Give the position of every malaria parasite and every leukocyte.
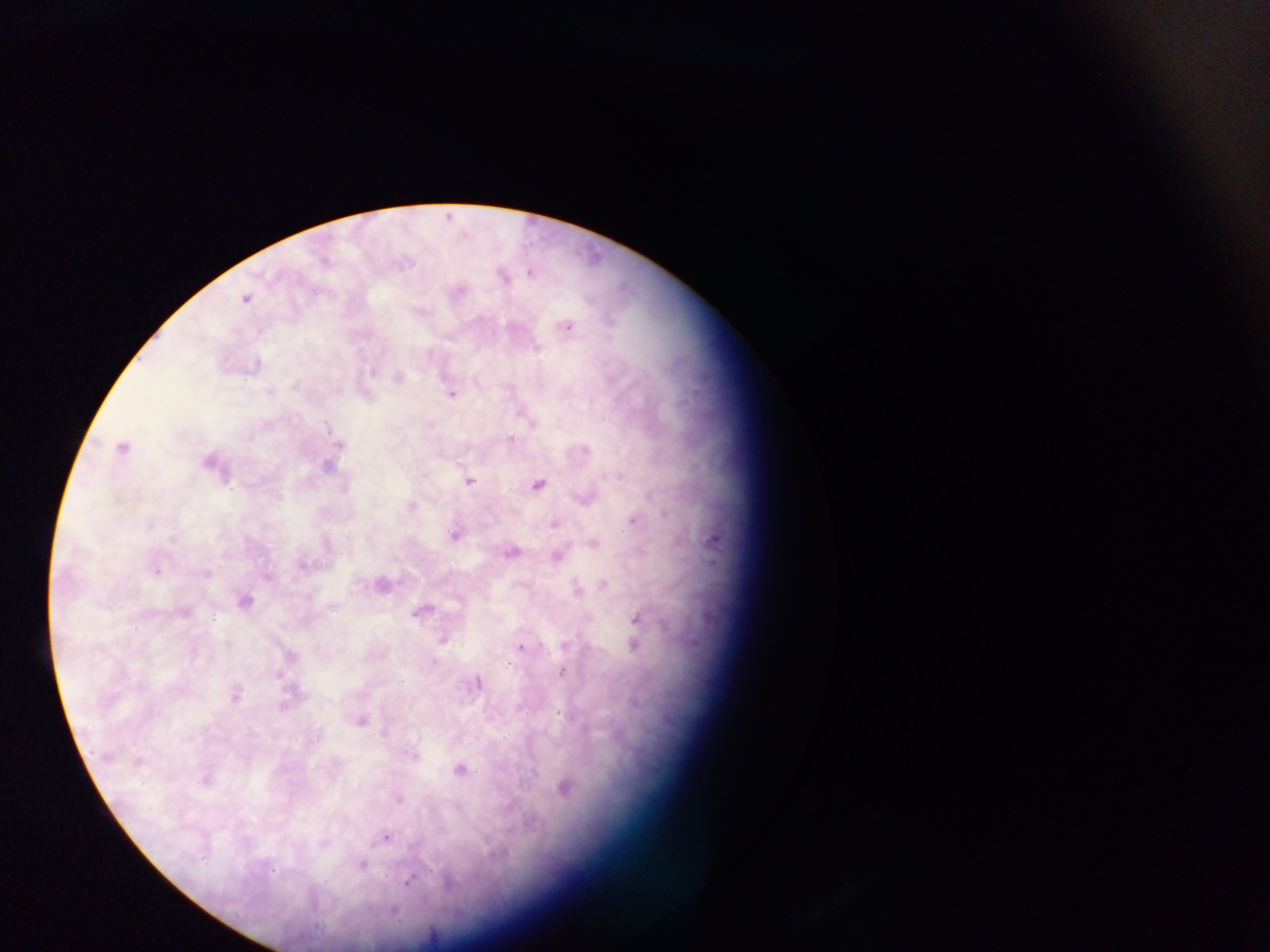
Approximate centers as (x, y) in pixels.
Malaria parasites: (530, 272), (504, 278), (244, 300), (567, 327), (537, 348), (373, 373), (399, 378), (294, 387), (269, 391), (451, 394), (328, 429), (510, 438), (339, 445), (123, 449), (585, 450), (208, 462), (326, 466), (620, 476), (470, 481), (539, 485), (410, 507), (633, 521), (150, 524), (554, 524), (454, 535), (348, 537), (173, 539), (593, 543), (512, 553), (557, 556), (302, 565), (156, 571), (206, 573), (267, 577), (603, 585), (577, 592), (244, 601), (332, 607), (184, 611), (421, 612), (213, 619), (639, 620), (443, 639), (226, 644), (634, 645), (565, 646), (521, 647), (290, 656), (433, 661), (508, 665), (561, 672), (276, 676), (478, 683), (235, 695), (361, 721), (411, 756), (138, 762), (459, 770), (204, 781), (565, 788), (398, 800), (385, 837), (323, 843), (362, 865), (272, 870), (409, 881), (448, 885), (394, 912), (316, 926).
No leukocytes observed.

Summary:
  - Image size: 1270×952 pixels
  - Capture: mobile-phone photograph through a microscope
  - Country: Ghana
  - Field of view: single
  - Preparation: thick blood smear